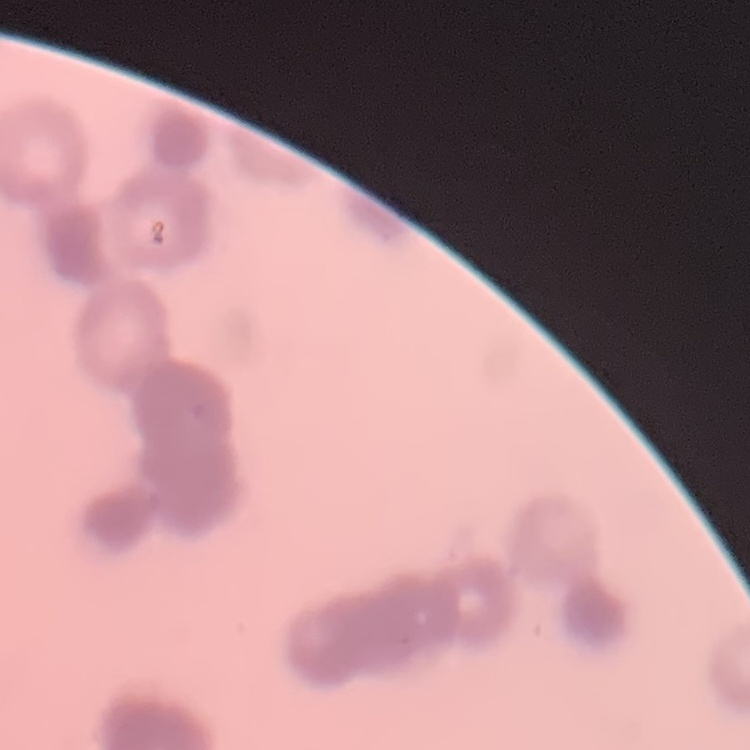
The erythrocytes show rouleaux formation. Square crop of a larger photomicrograph. Field's or Giemsa stain. Thin blood smear.